State which parasite is depicted.
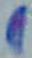
Toxoplasma gondii.

1000x magnification. Photomicrograph.